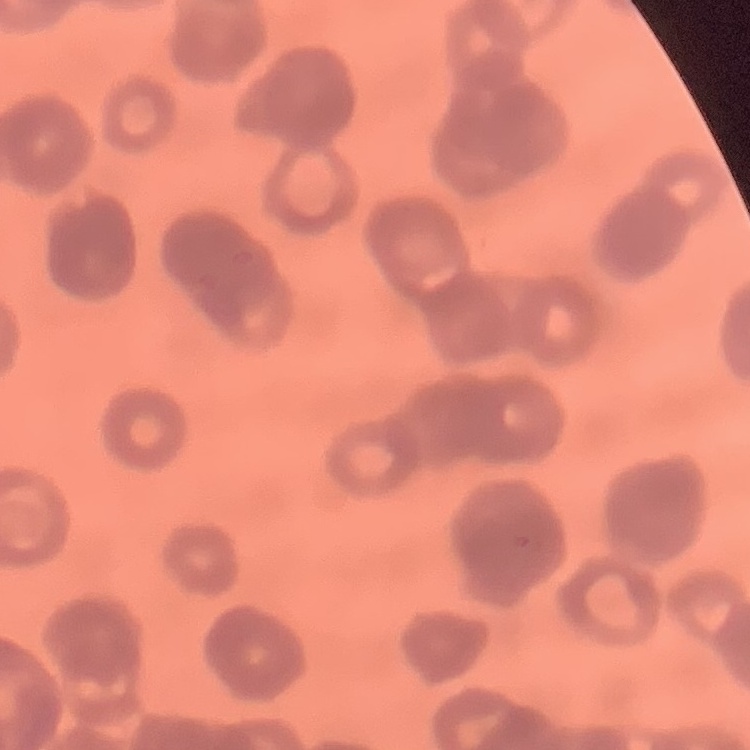
Summary:
  - Erythrocyte morphology: rouleaux formation
  - Preparation: thin peripheral smear
  - Image type: one tile cut from a larger photomicrograph
  - Stain: Field's or Giemsa